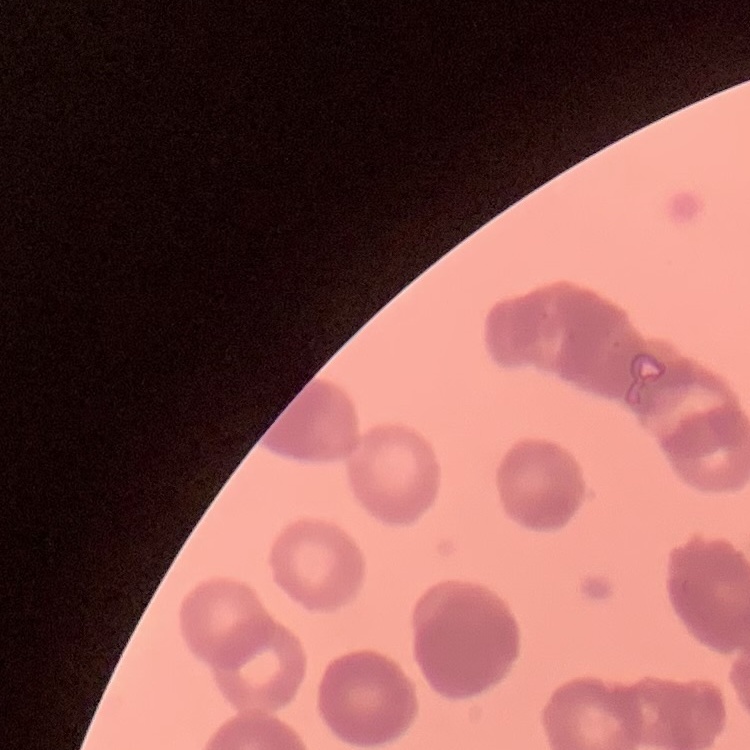
Summary:
  - Red blood cell morphology: rouleaux formation
  - Stain: Field's or Giemsa
  - Image type: one tile cut from a larger photomicrograph
  - Preparation: thin peripheral smear